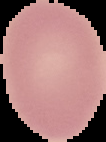
Summary:
  - Malaria status: uninfected
  - Image type: cell region segmented out of the field of view; surrounding area masked to black
  - Image size: 106×142 pixels
  - Preparation: thin blood film